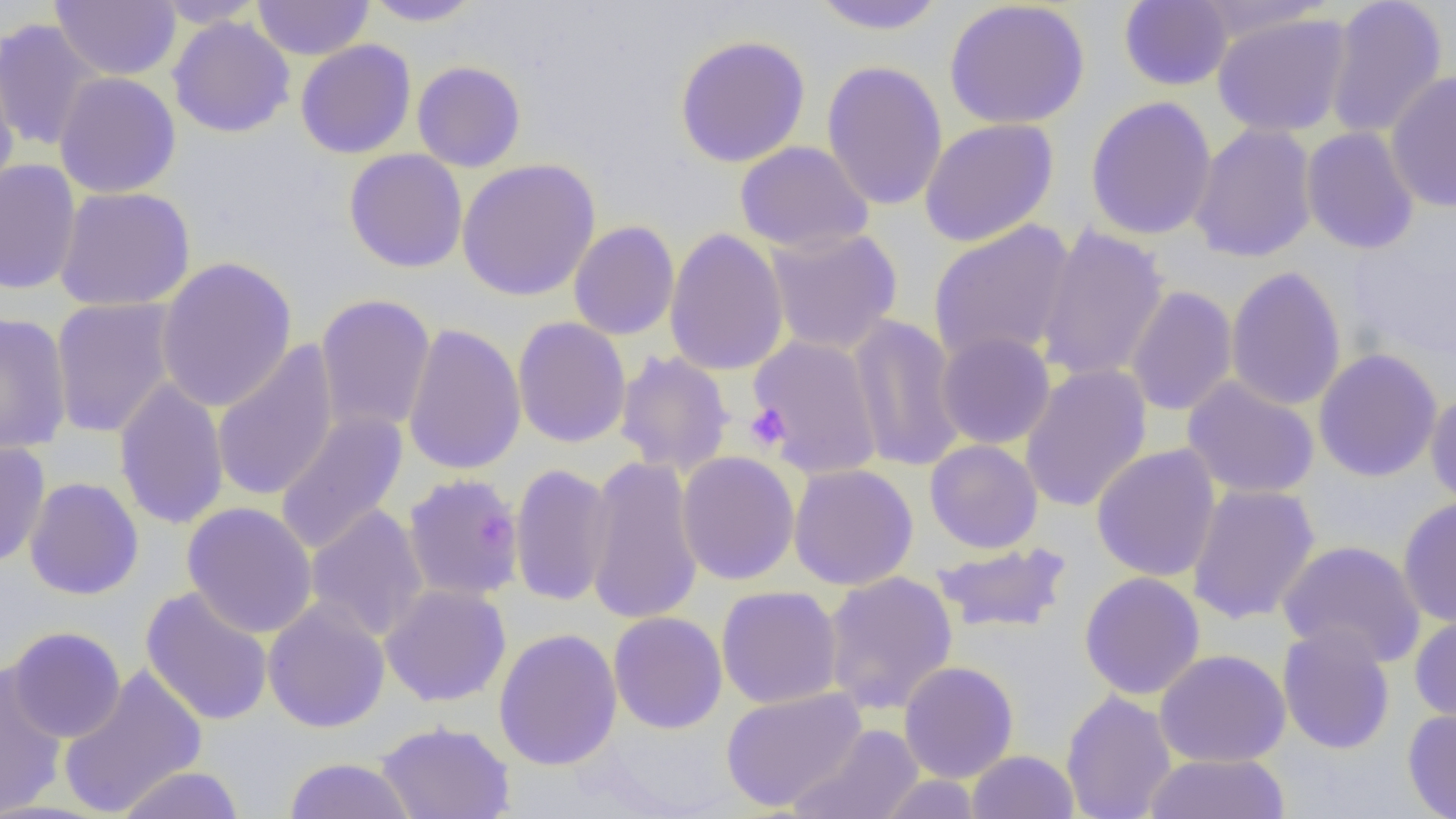

slide_level_diagnosis: no evidence of blood parasites
image_size: 1456×819 pixels
modality: optical microscopy
field_of_view: single
preparation: thin blood film
platelet_locations: 'approximate bounding boxes as [x1, y1, x2, y2] in pixels: [744, 404, 791, 451]'
magnification: 1000x
uninfected_red_blood_cell_locations: 'approximate bounding boxes as [x1, y1, x2, y2] in pixels: [50, 0, 181, 81], [153, 0, 268, 28], [252, 0, 374, 60], [361, 0, 485, 27], [807, 0, 949, 35], [1324, 0, 1448, 140], [944, 1, 1091, 130], [1118, 1, 1233, 91], [1191, 1, 1340, 44], [1212, 12, 1352, 137], [167, 15, 295, 138], [0, 18, 105, 153], [674, 34, 811, 168], [295, 40, 416, 159], [0, 50, 20, 201], [412, 60, 526, 172], [822, 60, 948, 212], [1386, 70, 1456, 213], [54, 71, 181, 199], [1084, 95, 1217, 241], [919, 118, 1059, 247], [1189, 123, 1318, 263], [1301, 126, 1420, 255], [734, 140, 874, 254], [343, 149, 468, 273], [456, 158, 601, 301], [0, 159, 82, 295], [54, 186, 196, 312], [568, 220, 680, 340], [928, 220, 1076, 365], [1035, 225, 1170, 384], [664, 227, 790, 377], [764, 227, 903, 356], [155, 256, 298, 413], [1225, 265, 1346, 412], [1124, 285, 1238, 417], [315, 294, 436, 435], [49, 297, 180, 438], [0, 311, 73, 455], [847, 314, 966, 472], [512, 317, 631, 448], [402, 323, 527, 476], [936, 331, 1056, 450], [747, 335, 885, 478], [211, 340, 340, 502], [1313, 348, 1443, 482], [615, 350, 735, 477], [1019, 364, 1153, 513], [1181, 376, 1320, 500], [113, 378, 230, 530], [1425, 391, 1456, 509], [273, 410, 409, 556], [924, 439, 1043, 553], [0, 440, 51, 568], [1091, 443, 1221, 582], [676, 450, 800, 585], [584, 455, 704, 626], [509, 461, 615, 608], [788, 463, 919, 591], [401, 471, 524, 601], [24, 477, 144, 600], [1186, 483, 1321, 624], [1398, 497, 1456, 629], [181, 501, 319, 638], [305, 504, 429, 643], [1277, 540, 1427, 669], [931, 542, 1073, 635], [822, 570, 959, 715], [1078, 571, 1206, 700], [379, 583, 511, 707], [140, 585, 274, 726], [716, 585, 843, 709], [263, 599, 391, 734], [608, 611, 727, 734], [1409, 612, 1456, 729], [1277, 625, 1396, 755], [5, 626, 126, 743], [494, 628, 623, 771], [1154, 649, 1291, 768], [898, 660, 1019, 783], [0, 665, 69, 818], [57, 666, 208, 818], [721, 687, 868, 812], [1061, 689, 1177, 819], [1403, 707, 1456, 818], [376, 720, 516, 819], [789, 723, 924, 819], [967, 750, 1079, 819], [1145, 753, 1290, 818], [283, 757, 416, 819], [115, 765, 245, 819], [876, 775, 985, 818]'